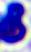
{
  "identification": "white blood cell",
  "modality": "photomicrograph",
  "magnification": "400x"
}